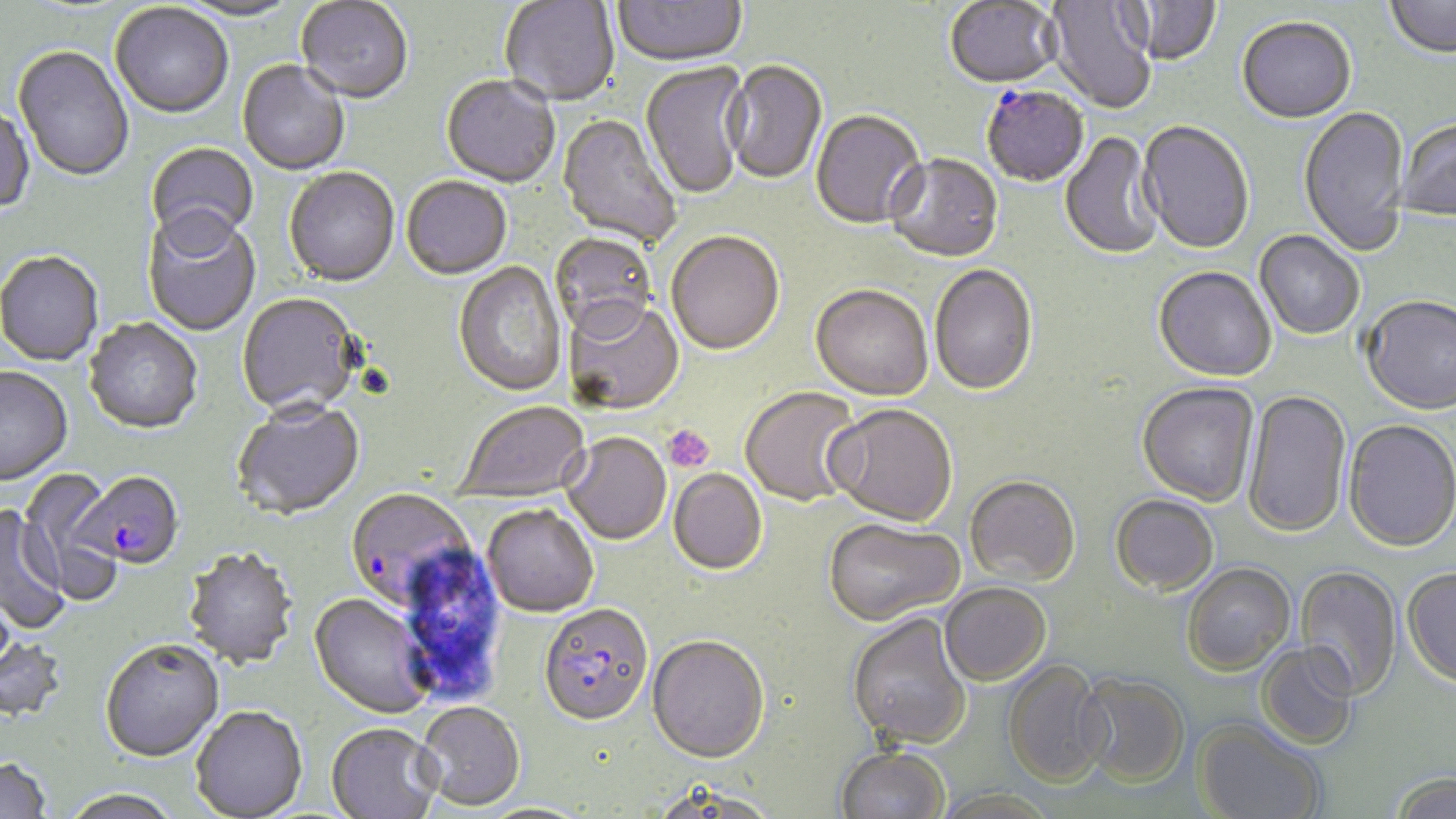

slide-level diagnosis = Plasmodium falciparum
stain = May-Grünwald-Giemsa
platelet locations = approximate bounding boxes as named x1/y1/x2/y2 corners in pixels: (x1=663, y1=424, x2=715, y2=472)
field of view = single
Plasmodium falciparum-infected red blood cell locations = approximate bounding boxes as named x1/y1/x2/y2 corners in pixels: (x1=981, y1=85, x2=1089, y2=187), (x1=75, y1=474, x2=183, y2=571), (x1=344, y1=488, x2=475, y2=610), (x1=538, y1=602, x2=653, y2=724)
image size = 1456×819 pixels
uninfected red blood cell locations = approximate bounding boxes as named x1/y1/x2/y2 corners in pixels: (x1=176, y1=0, x2=303, y2=23), (x1=500, y1=0, x2=620, y2=107), (x1=612, y1=0, x2=747, y2=68), (x1=1126, y1=0, x2=1222, y2=65), (x1=1385, y1=0, x2=1456, y2=59), (x1=296, y1=1, x2=413, y2=106), (x1=945, y1=1, x2=1061, y2=88), (x1=1044, y1=1, x2=1158, y2=114), (x1=110, y1=4, x2=233, y2=121), (x1=1237, y1=15, x2=1356, y2=122), (x1=13, y1=47, x2=134, y2=184), (x1=724, y1=60, x2=828, y2=186), (x1=237, y1=61, x2=350, y2=176), (x1=639, y1=62, x2=751, y2=201), (x1=441, y1=77, x2=560, y2=189), (x1=1298, y1=105, x2=1410, y2=256), (x1=0, y1=106, x2=34, y2=217), (x1=810, y1=109, x2=926, y2=229), (x1=557, y1=113, x2=683, y2=248), (x1=1396, y1=116, x2=1456, y2=221), (x1=1138, y1=119, x2=1255, y2=253), (x1=1061, y1=131, x2=1162, y2=260), (x1=146, y1=142, x2=260, y2=252), (x1=885, y1=152, x2=1003, y2=261), (x1=284, y1=168, x2=400, y2=288), (x1=401, y1=177, x2=511, y2=281), (x1=142, y1=212, x2=261, y2=337), (x1=665, y1=230, x2=785, y2=354), (x1=1255, y1=230, x2=1365, y2=339), (x1=550, y1=232, x2=658, y2=339), (x1=0, y1=253, x2=104, y2=367), (x1=454, y1=262, x2=567, y2=397), (x1=930, y1=263, x2=1038, y2=395), (x1=1154, y1=265, x2=1277, y2=381), (x1=810, y1=283, x2=933, y2=400), (x1=237, y1=294, x2=363, y2=418), (x1=1361, y1=294, x2=1456, y2=414), (x1=562, y1=298, x2=684, y2=415), (x1=84, y1=319, x2=203, y2=436), (x1=0, y1=367, x2=73, y2=487), (x1=1137, y1=382, x2=1259, y2=505), (x1=739, y1=385, x2=862, y2=507), (x1=1242, y1=389, x2=1351, y2=538), (x1=455, y1=400, x2=590, y2=502), (x1=231, y1=401, x2=365, y2=521), (x1=826, y1=402, x2=958, y2=525), (x1=1343, y1=418, x2=1456, y2=552), (x1=562, y1=432, x2=671, y2=544), (x1=669, y1=468, x2=767, y2=574), (x1=16, y1=471, x2=119, y2=602), (x1=964, y1=474, x2=1081, y2=586), (x1=1111, y1=493, x2=1219, y2=594), (x1=483, y1=503, x2=599, y2=617), (x1=0, y1=506, x2=68, y2=634), (x1=823, y1=517, x2=964, y2=626), (x1=182, y1=548, x2=298, y2=671), (x1=1181, y1=561, x2=1295, y2=675), (x1=1295, y1=565, x2=1402, y2=700), (x1=1402, y1=565, x2=1456, y2=685), (x1=939, y1=582, x2=1051, y2=685), (x1=309, y1=593, x2=434, y2=720), (x1=846, y1=611, x2=973, y2=749), (x1=647, y1=633, x2=770, y2=762), (x1=0, y1=638, x2=68, y2=723), (x1=100, y1=641, x2=224, y2=764), (x1=1256, y1=642, x2=1360, y2=749), (x1=1001, y1=659, x2=1111, y2=787), (x1=1077, y1=673, x2=1191, y2=787), (x1=414, y1=701, x2=525, y2=810), (x1=190, y1=707, x2=307, y2=819), (x1=1194, y1=718, x2=1326, y2=819), (x1=326, y1=722, x2=442, y2=818), (x1=834, y1=744, x2=950, y2=819), (x1=0, y1=758, x2=52, y2=818), (x1=1388, y1=771, x2=1456, y2=818), (x1=650, y1=780, x2=780, y2=819), (x1=59, y1=791, x2=185, y2=819), (x1=476, y1=802, x2=596, y2=819)
preparation = thin blood film
modality = optical microscopy
magnification = 1000x